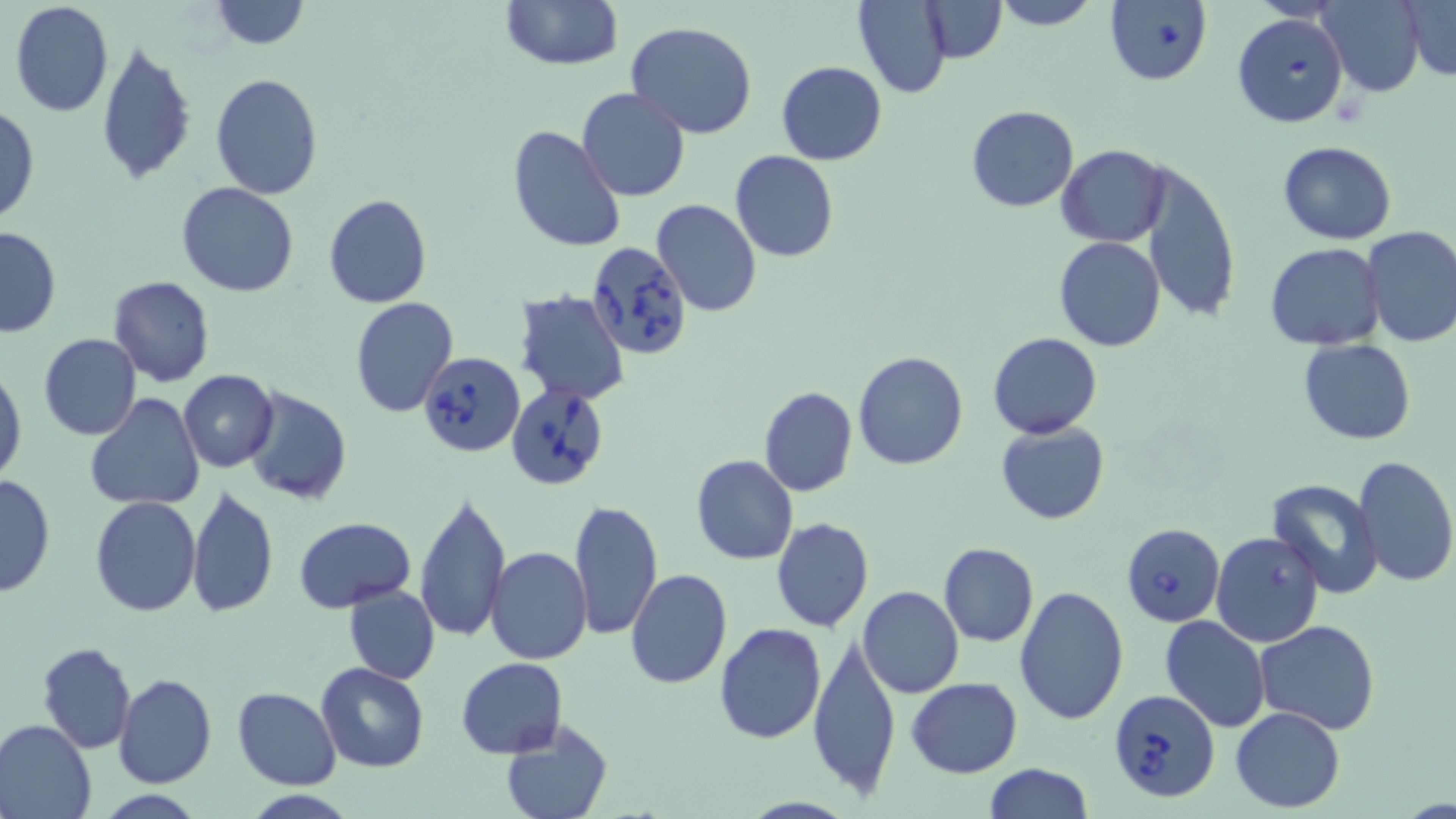
Summary:
  - Coordinate format: approximate bounding boxes as (x1,y1)-(x2,y2) corner pairs in pixels
  - Uninfected red blood cell locations: (209,0)-(308,50), (497,0)-(624,71), (919,0)-(1007,62), (989,0)-(1101,30), (1320,0)-(1424,96), (1402,1)-(1456,79), (8,2)-(114,117), (853,2)-(952,98), (625,20)-(758,140), (95,39)-(197,185), (776,61)-(887,166), (210,72)-(323,199), (577,87)-(690,202), (0,104)-(39,226), (966,105)-(1078,212), (506,126)-(626,253), (1277,141)-(1396,246), (1057,145)-(1171,247), (730,150)-(840,262), (1138,161)-(1240,321), (176,182)-(301,297), (322,193)-(433,309), (652,200)-(762,316), (0,226)-(61,338), (1359,226)-(1456,347), (1053,237)-(1167,352), (1264,243)-(1386,349), (107,276)-(215,387), (514,290)-(631,407), (350,298)-(458,417), (37,332)-(143,441), (988,332)-(1102,438), (1299,339)-(1416,444), (853,350)-(968,470), (0,366)-(25,484), (179,369)-(278,472), (243,386)-(352,505), (759,386)-(858,497), (83,393)-(204,512), (996,422)-(1108,525), (690,454)-(798,565), (1353,455)-(1456,588), (0,472)-(56,597), (1267,478)-(1385,598), (186,485)-(279,618), (414,490)-(510,644), (89,494)-(200,618), (569,499)-(662,641), (293,516)-(417,612), (771,517)-(874,634), (1211,529)-(1324,647), (939,542)-(1038,648), (488,546)-(593,664), (625,569)-(732,690), (342,584)-(440,683), (1013,584)-(1130,725), (859,586)-(964,698), (1158,616)-(1271,732), (1255,619)-(1381,734), (714,622)-(826,744), (806,633)-(901,799), (37,642)-(137,753), (456,656)-(567,758), (315,661)-(428,773), (115,674)-(218,789), (906,677)-(1022,778), (231,687)-(342,789), (1230,706)-(1347,812), (0,719)-(96,819), (500,720)-(614,819), (981,763)-(1093,819), (239,791)-(361,819)
  - Babesia divergens-infected red blood cell locations: (1104,0)-(1214,86), (1232,12)-(1350,128), (586,241)-(694,362), (419,350)-(524,456), (507,384)-(608,490), (1121,523)-(1224,627), (1107,688)-(1219,804)
  - Slide-level diagnosis: Babesia divergens
  - Preparation: thin blood film
  - Modality: optical microscopy
  - Stain: May-Grünwald-Giemsa
  - Field of view: single
  - Magnification: 1000x
  - Image size: 1456×819 pixels